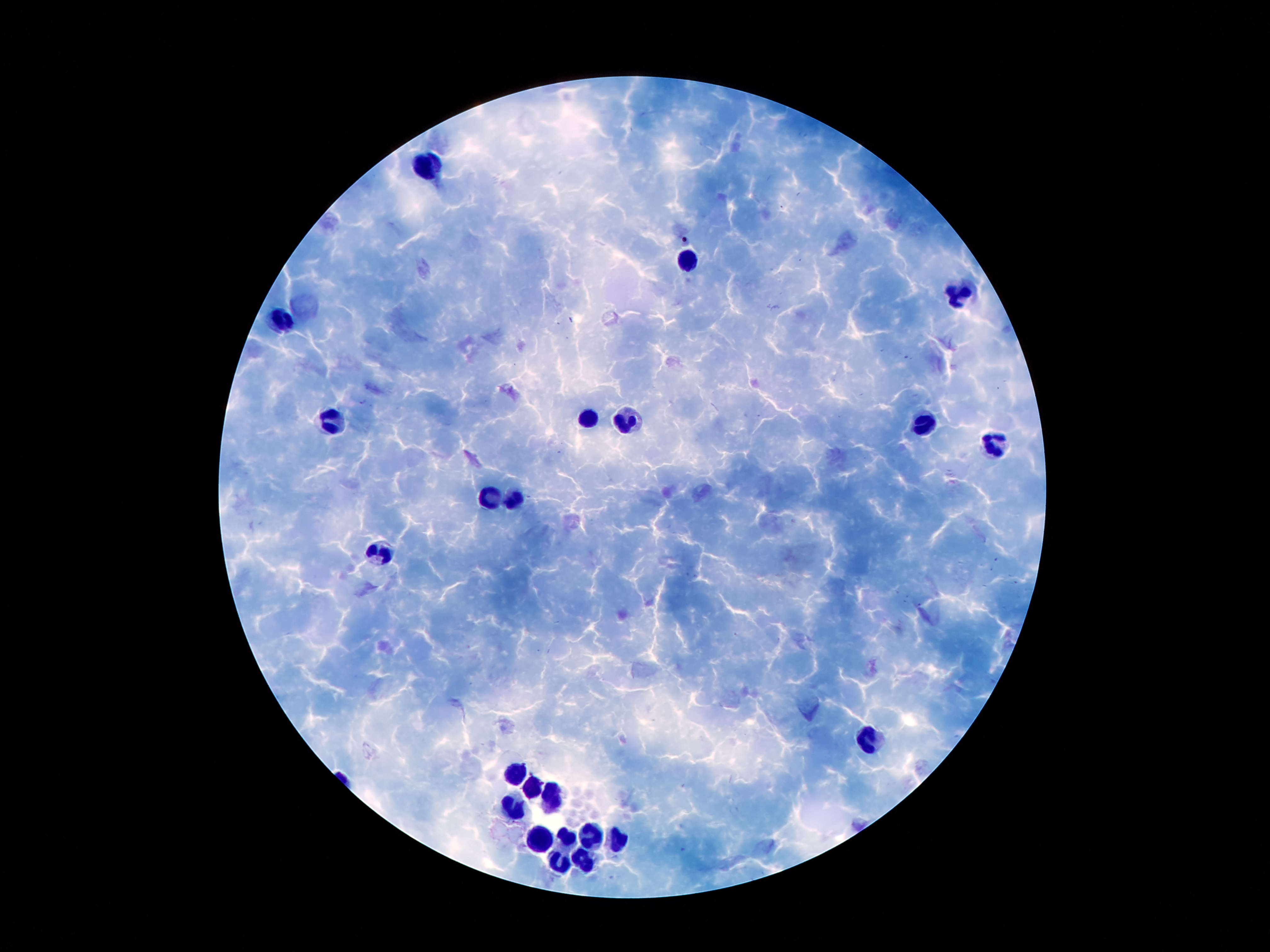
Approximate centers as (x, y) in pixels.
Summary:
  - Leukocyte locations: (428, 167), (687, 262), (959, 291), (283, 322), (590, 418), (623, 421), (335, 424), (923, 425), (993, 447), (516, 499), (489, 500), (379, 554), (865, 742), (513, 774), (536, 787), (548, 796), (513, 810), (593, 836), (538, 841), (564, 841), (619, 841), (590, 862), (559, 864)
  - Plasmodium parasite locations: (685, 240), (363, 401)
  - Magnification: 100x
  - Preparation: thick blood smear
  - Patient malaria status: infected with Plasmodium falciparum
  - Field of view: one from this slide
  - Stain: Giemsa
  - Capture: smartphone through the microscope eyepiece
  - Image size: 1270×952 pixels